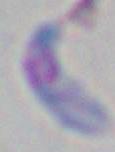

modality: photomicrograph
magnification: 1000x
identification: Toxoplasma gondii